Classify this cell by malaria status.
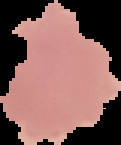

It is uninfected.

Summary:
  - Preparation: thin blood smear
  - Image size: 121×145 pixels
  - Image type: segmented cell region on a black background